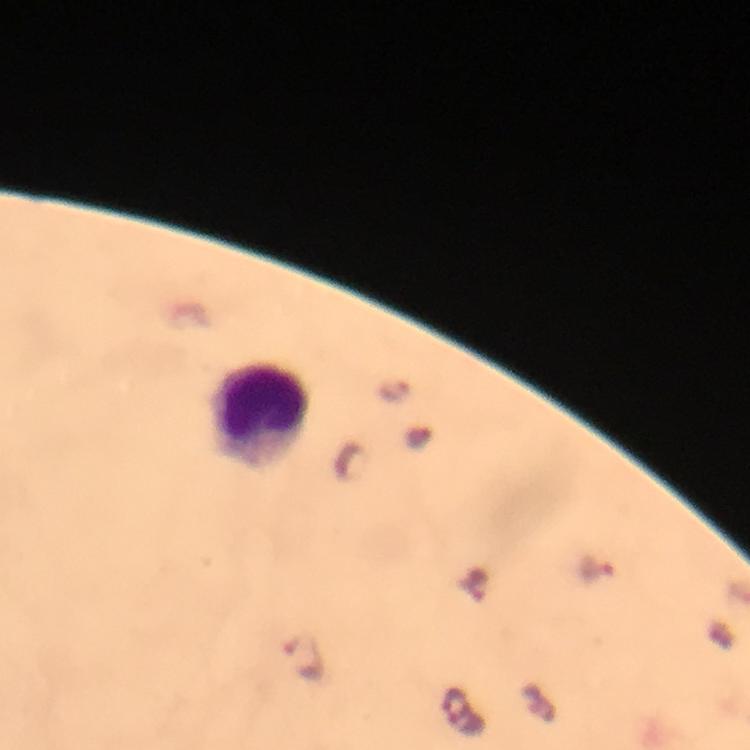

Approximate centers as (x, y) in pixels. Leukocyte locations: (260, 411). Malaria parasite locations: (395, 391), (596, 569), (306, 654). At 100x magnification. Immersion oil was used. Giemsa-stained preparation. From a malaria diagnostic workup. Smartphone photograph taken through a microscope. Thick smear. Image is 750×750 pixels. A crop from one field of view.